Give the extent of all uninfected red blood cells.
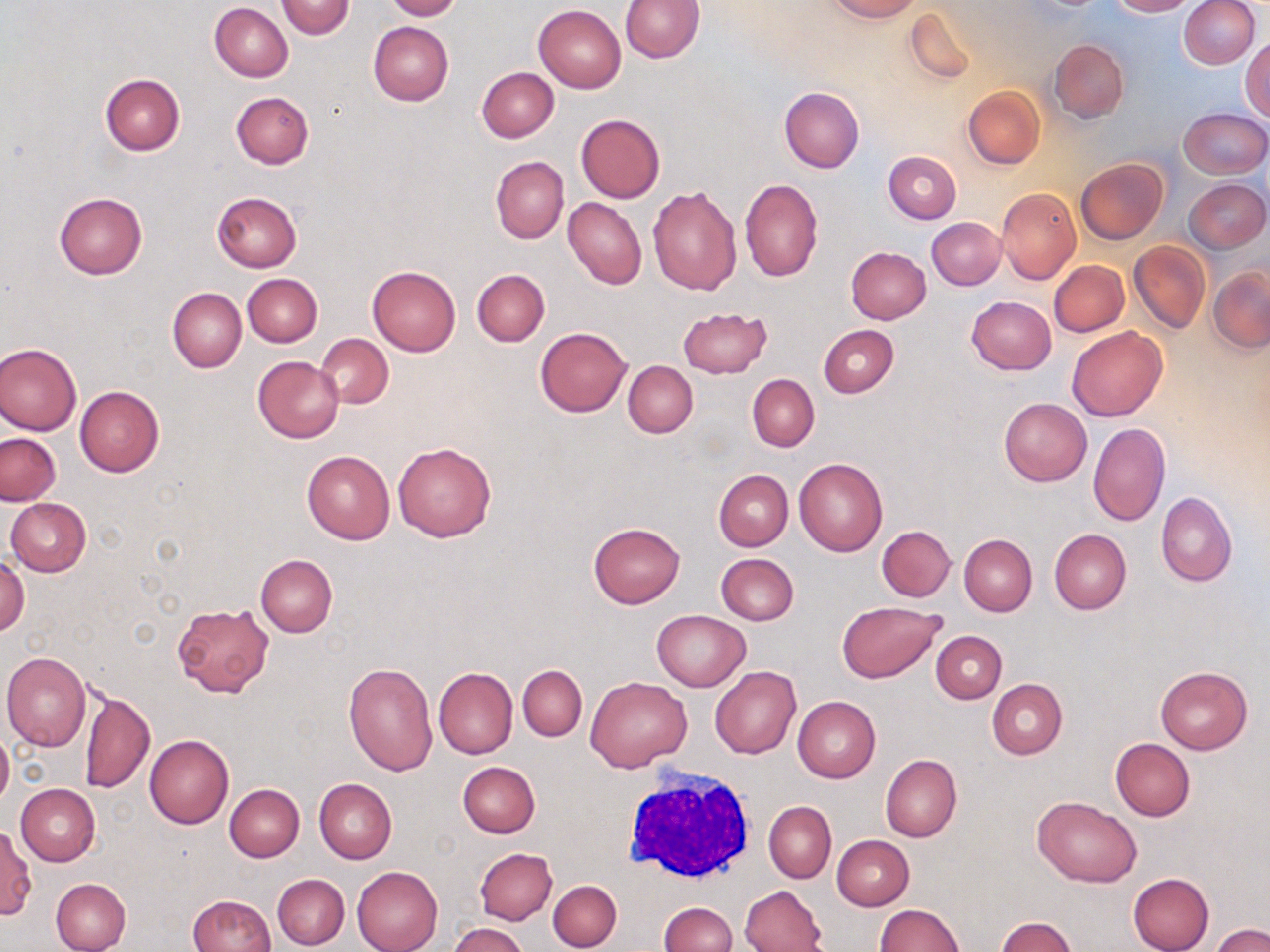
Approximate bounding boxes as named x1/y1/x2/y2 corners in pixels.
Uninfected red blood cells: (x1=382, y1=0, x2=461, y2=20), (x1=828, y1=0, x2=920, y2=21), (x1=1106, y1=0, x2=1195, y2=16), (x1=1177, y1=0, x2=1259, y2=70), (x1=276, y1=1, x2=354, y2=38), (x1=620, y1=1, x2=704, y2=63), (x1=209, y1=4, x2=293, y2=82), (x1=534, y1=4, x2=626, y2=92), (x1=904, y1=6, x2=977, y2=84), (x1=368, y1=21, x2=453, y2=105), (x1=1241, y1=35, x2=1270, y2=119), (x1=1049, y1=38, x2=1129, y2=123), (x1=477, y1=67, x2=559, y2=142), (x1=99, y1=75, x2=184, y2=156), (x1=779, y1=86, x2=864, y2=174), (x1=963, y1=86, x2=1045, y2=169), (x1=231, y1=91, x2=314, y2=168), (x1=1179, y1=108, x2=1269, y2=179), (x1=576, y1=114, x2=665, y2=202), (x1=883, y1=151, x2=961, y2=223), (x1=490, y1=156, x2=568, y2=244), (x1=1076, y1=158, x2=1167, y2=243), (x1=740, y1=179, x2=823, y2=281), (x1=1185, y1=179, x2=1268, y2=253), (x1=647, y1=185, x2=742, y2=296), (x1=996, y1=187, x2=1080, y2=285), (x1=54, y1=191, x2=147, y2=278), (x1=212, y1=192, x2=302, y2=272), (x1=564, y1=197, x2=646, y2=289), (x1=928, y1=217, x2=1004, y2=289), (x1=1129, y1=242, x2=1210, y2=335), (x1=844, y1=246, x2=931, y2=323), (x1=1050, y1=260, x2=1129, y2=336), (x1=367, y1=267, x2=461, y2=356), (x1=1209, y1=267, x2=1269, y2=351), (x1=472, y1=269, x2=550, y2=345), (x1=242, y1=274, x2=322, y2=347), (x1=168, y1=288, x2=247, y2=372), (x1=967, y1=296, x2=1056, y2=375), (x1=677, y1=306, x2=772, y2=378), (x1=818, y1=324, x2=899, y2=398), (x1=1066, y1=326, x2=1167, y2=422), (x1=535, y1=327, x2=631, y2=417), (x1=318, y1=334, x2=393, y2=408), (x1=0, y1=342, x2=82, y2=436), (x1=253, y1=356, x2=344, y2=443), (x1=623, y1=361, x2=698, y2=438), (x1=747, y1=374, x2=819, y2=452), (x1=74, y1=385, x2=165, y2=477), (x1=998, y1=397, x2=1092, y2=486), (x1=1089, y1=422, x2=1170, y2=526), (x1=1, y1=433, x2=61, y2=506), (x1=393, y1=442, x2=495, y2=542), (x1=302, y1=450, x2=395, y2=544), (x1=794, y1=458, x2=887, y2=555), (x1=714, y1=470, x2=793, y2=552), (x1=1156, y1=492, x2=1237, y2=587), (x1=6, y1=499, x2=91, y2=576), (x1=588, y1=523, x2=685, y2=608), (x1=876, y1=526, x2=956, y2=601), (x1=1049, y1=528, x2=1131, y2=615), (x1=959, y1=534, x2=1037, y2=616), (x1=0, y1=553, x2=30, y2=637), (x1=716, y1=553, x2=798, y2=626), (x1=255, y1=555, x2=337, y2=637), (x1=836, y1=600, x2=947, y2=683), (x1=172, y1=603, x2=273, y2=697), (x1=652, y1=610, x2=750, y2=691), (x1=931, y1=630, x2=1007, y2=702), (x1=2, y1=652, x2=90, y2=751), (x1=345, y1=662, x2=437, y2=777), (x1=518, y1=665, x2=586, y2=740), (x1=710, y1=666, x2=801, y2=759), (x1=433, y1=667, x2=518, y2=758), (x1=1155, y1=667, x2=1251, y2=754), (x1=586, y1=677, x2=692, y2=772), (x1=987, y1=679, x2=1067, y2=758), (x1=79, y1=689, x2=154, y2=794), (x1=792, y1=696, x2=881, y2=782), (x1=0, y1=730, x2=13, y2=808), (x1=144, y1=735, x2=233, y2=828), (x1=1111, y1=738, x2=1195, y2=822), (x1=881, y1=754, x2=962, y2=842), (x1=457, y1=761, x2=540, y2=838), (x1=314, y1=778, x2=397, y2=863), (x1=225, y1=783, x2=304, y2=861), (x1=16, y1=784, x2=100, y2=865), (x1=1031, y1=796, x2=1142, y2=887), (x1=764, y1=801, x2=836, y2=883), (x1=0, y1=825, x2=35, y2=918), (x1=832, y1=834, x2=915, y2=911), (x1=474, y1=848, x2=557, y2=924), (x1=352, y1=866, x2=443, y2=952), (x1=1127, y1=873, x2=1214, y2=952), (x1=273, y1=874, x2=350, y2=949), (x1=50, y1=878, x2=131, y2=952), (x1=548, y1=880, x2=621, y2=950), (x1=739, y1=884, x2=826, y2=952), (x1=188, y1=894, x2=275, y2=952), (x1=658, y1=894, x2=821, y2=952), (x1=658, y1=902, x2=736, y2=952), (x1=874, y1=904, x2=964, y2=952), (x1=994, y1=917, x2=1077, y2=951), (x1=449, y1=923, x2=529, y2=952), (x1=1213, y1=924, x2=1269, y2=952).

White blood cell locations: (x1=619, y1=766, x2=759, y2=886). Slide-level diagnosis: negative for blood parasites. Captured at 1000x magnification. Thin blood film. Image is 1270×952 pixels. Optical microscopy. Single field of view. May-Grünwald-Giemsa stain.